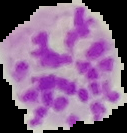
image size = 127×133 pixels
preparation = thin blood film
image type = segmented cell region on a black background
malaria status = parasitized